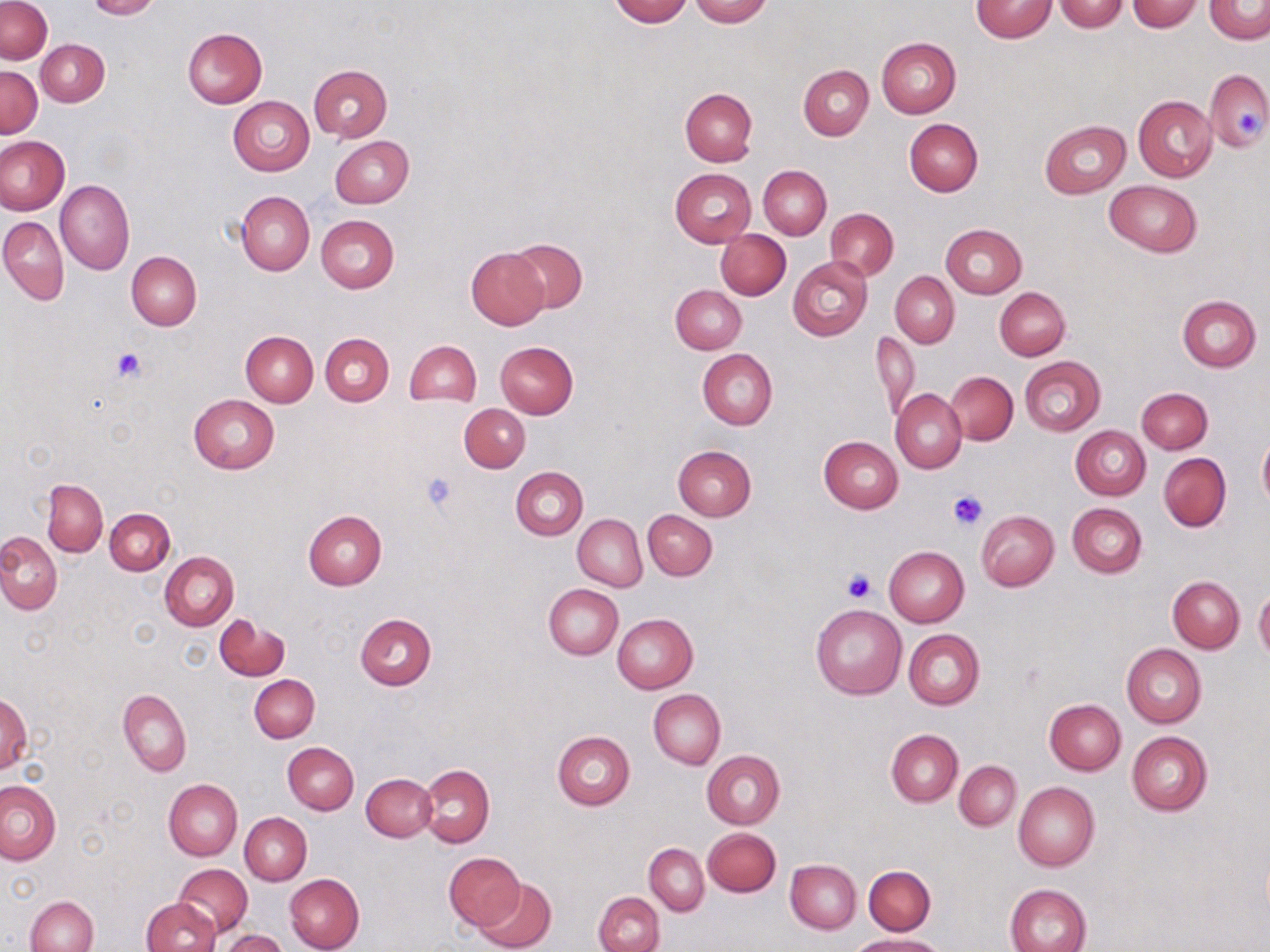

Approximate bounding boxes as named x1/y1/x2/y2 corners in pixels. Uninfected red blood cell locations: (x1=0, y1=0, x2=52, y2=64), (x1=85, y1=0, x2=159, y2=19), (x1=609, y1=0, x2=693, y2=26), (x1=689, y1=0, x2=772, y2=27), (x1=971, y1=1, x2=1056, y2=42), (x1=1054, y1=1, x2=1130, y2=32), (x1=1126, y1=1, x2=1201, y2=32), (x1=1204, y1=1, x2=1270, y2=43), (x1=183, y1=28, x2=266, y2=107), (x1=877, y1=36, x2=961, y2=118), (x1=37, y1=39, x2=109, y2=107), (x1=798, y1=64, x2=873, y2=139), (x1=308, y1=65, x2=392, y2=141), (x1=0, y1=66, x2=42, y2=138), (x1=1204, y1=68, x2=1270, y2=151), (x1=680, y1=88, x2=758, y2=165), (x1=1133, y1=94, x2=1217, y2=182), (x1=228, y1=96, x2=314, y2=177), (x1=905, y1=117, x2=983, y2=196), (x1=1040, y1=120, x2=1131, y2=198), (x1=0, y1=135, x2=69, y2=215), (x1=330, y1=135, x2=413, y2=208), (x1=758, y1=165, x2=831, y2=239), (x1=670, y1=168, x2=757, y2=246), (x1=55, y1=179, x2=134, y2=275), (x1=1104, y1=181, x2=1202, y2=256), (x1=236, y1=190, x2=314, y2=276), (x1=825, y1=209, x2=898, y2=280), (x1=316, y1=214, x2=399, y2=293), (x1=0, y1=216, x2=68, y2=305), (x1=940, y1=224, x2=1027, y2=298), (x1=717, y1=230, x2=791, y2=300), (x1=505, y1=237, x2=587, y2=314), (x1=464, y1=247, x2=550, y2=330), (x1=127, y1=251, x2=202, y2=330), (x1=788, y1=256, x2=872, y2=341), (x1=891, y1=271, x2=959, y2=347), (x1=671, y1=285, x2=746, y2=354), (x1=995, y1=287, x2=1069, y2=360), (x1=1177, y1=295, x2=1260, y2=372), (x1=241, y1=330, x2=318, y2=406), (x1=873, y1=330, x2=920, y2=424), (x1=321, y1=333, x2=393, y2=405), (x1=403, y1=340, x2=481, y2=407), (x1=495, y1=341, x2=578, y2=418), (x1=697, y1=348, x2=778, y2=429), (x1=1019, y1=356, x2=1106, y2=436), (x1=945, y1=372, x2=1018, y2=444), (x1=1136, y1=387, x2=1211, y2=454), (x1=892, y1=390, x2=966, y2=474), (x1=188, y1=394, x2=280, y2=474), (x1=459, y1=404, x2=530, y2=472), (x1=1071, y1=425, x2=1150, y2=500), (x1=819, y1=435, x2=903, y2=512), (x1=1257, y1=435, x2=1270, y2=511), (x1=673, y1=445, x2=757, y2=521), (x1=1159, y1=452, x2=1231, y2=531), (x1=511, y1=466, x2=588, y2=540), (x1=43, y1=479, x2=107, y2=556), (x1=1067, y1=503, x2=1146, y2=578), (x1=105, y1=508, x2=174, y2=575), (x1=643, y1=509, x2=717, y2=580), (x1=304, y1=510, x2=387, y2=590), (x1=977, y1=511, x2=1059, y2=591), (x1=573, y1=514, x2=647, y2=590), (x1=0, y1=534, x2=62, y2=613), (x1=884, y1=546, x2=968, y2=628), (x1=160, y1=551, x2=239, y2=631), (x1=1167, y1=576, x2=1244, y2=652), (x1=543, y1=585, x2=622, y2=660), (x1=1254, y1=588, x2=1270, y2=662), (x1=810, y1=604, x2=907, y2=699), (x1=355, y1=613, x2=437, y2=690), (x1=612, y1=614, x2=697, y2=693), (x1=215, y1=617, x2=289, y2=681), (x1=903, y1=629, x2=984, y2=711), (x1=1121, y1=644, x2=1205, y2=728), (x1=249, y1=675, x2=319, y2=742), (x1=118, y1=689, x2=192, y2=776), (x1=649, y1=690, x2=726, y2=768), (x1=1, y1=695, x2=32, y2=774), (x1=1044, y1=699, x2=1125, y2=774), (x1=886, y1=729, x2=963, y2=806), (x1=552, y1=730, x2=635, y2=810), (x1=1126, y1=731, x2=1213, y2=815), (x1=283, y1=742, x2=359, y2=814), (x1=702, y1=750, x2=784, y2=829), (x1=955, y1=761, x2=1021, y2=831), (x1=417, y1=764, x2=495, y2=847), (x1=362, y1=773, x2=437, y2=842), (x1=163, y1=779, x2=242, y2=861), (x1=0, y1=780, x2=61, y2=864), (x1=1013, y1=781, x2=1099, y2=871), (x1=240, y1=812, x2=312, y2=885), (x1=702, y1=828, x2=781, y2=897), (x1=644, y1=842, x2=709, y2=915), (x1=444, y1=851, x2=521, y2=930), (x1=785, y1=859, x2=861, y2=934), (x1=176, y1=865, x2=252, y2=937), (x1=863, y1=865, x2=936, y2=935), (x1=285, y1=873, x2=365, y2=952), (x1=474, y1=877, x2=556, y2=952), (x1=1005, y1=883, x2=1093, y2=952), (x1=594, y1=892, x2=664, y2=952), (x1=25, y1=895, x2=98, y2=952), (x1=141, y1=897, x2=219, y2=952), (x1=219, y1=929, x2=288, y2=951), (x1=851, y1=933, x2=944, y2=951). Platelet locations: (x1=1237, y1=112, x2=1261, y2=138), (x1=109, y1=346, x2=148, y2=384), (x1=422, y1=473, x2=458, y2=513), (x1=947, y1=489, x2=989, y2=531), (x1=841, y1=569, x2=875, y2=603). Slide-level diagnosis: no evidence of blood parasites. 1000x magnification. One field of a larger specimen. Thin blood film. Light microscopy. May-Grünwald-Giemsa-stained preparation. Image is 1270×952 pixels.